Locate every Trypanosoma brucei.
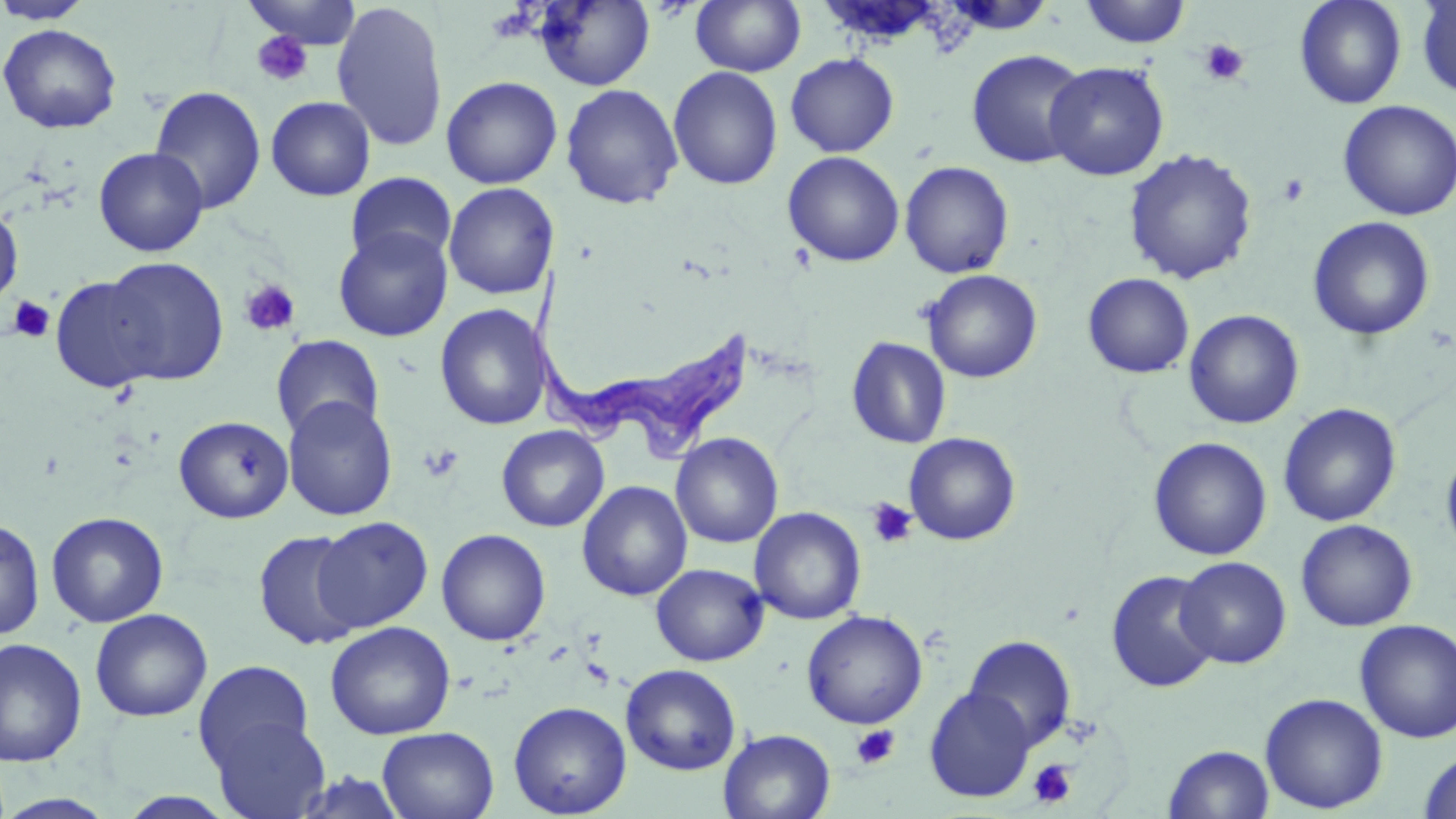

Approximate bounding boxes as (x1, y1, x2, y2) in pixels.
Trypanosoma brucei: (529, 266, 758, 463).

Uninfected red blood cell locations: (0, 0, 95, 25), (242, 0, 362, 49), (533, 0, 655, 91), (691, 0, 806, 77), (941, 0, 1055, 35), (1294, 0, 1407, 109), (1415, 0, 1456, 100), (1079, 1, 1191, 48), (332, 2, 448, 152), (0, 24, 122, 134), (966, 49, 1089, 169), (785, 53, 899, 157), (1044, 61, 1169, 181), (668, 66, 783, 190), (441, 76, 562, 189), (560, 83, 683, 210), (149, 86, 266, 215), (266, 96, 375, 201), (1338, 99, 1456, 221), (94, 147, 208, 256), (1123, 148, 1258, 285), (782, 151, 905, 267), (900, 160, 1015, 279), (345, 172, 457, 270), (443, 183, 559, 299), (0, 205, 23, 309), (1307, 216, 1435, 341), (333, 226, 453, 342), (100, 256, 229, 385), (922, 269, 1042, 383), (1082, 273, 1194, 378), (51, 276, 166, 392), (435, 303, 550, 431), (1184, 309, 1304, 429), (270, 334, 384, 439), (846, 336, 952, 449), (283, 397, 397, 521), (1278, 403, 1401, 527), (174, 415, 294, 523), (496, 425, 609, 532), (670, 432, 783, 548), (903, 432, 1020, 545), (1148, 437, 1272, 561), (1440, 448, 1456, 560), (576, 480, 692, 601), (750, 507, 866, 625), (46, 511, 169, 628), (313, 516, 433, 632), (0, 517, 45, 641), (1295, 519, 1418, 631), (252, 529, 364, 650), (436, 529, 551, 646), (1174, 556, 1291, 669), (650, 563, 768, 666), (1105, 570, 1221, 693), (89, 608, 213, 722), (801, 609, 928, 729), (1353, 618, 1456, 744), (325, 621, 456, 740), (963, 635, 1077, 750), (0, 638, 88, 767), (193, 660, 314, 774), (621, 663, 741, 775), (924, 686, 1036, 802), (1260, 692, 1388, 814), (508, 700, 632, 818), (209, 714, 331, 819), (378, 726, 499, 819), (718, 728, 836, 819), (1164, 744, 1274, 819), (1418, 750, 1456, 819), (112, 791, 243, 818), (0, 793, 118, 819). Platelet locations: (251, 30, 314, 87), (1199, 39, 1249, 85), (1278, 174, 1310, 205), (238, 279, 302, 337), (7, 295, 56, 342), (419, 444, 463, 482), (865, 497, 917, 549), (850, 724, 900, 770), (1028, 759, 1077, 808). Slide-level diagnosis: Trypanosoma brucei. Captured at 1000x magnification. May-Grünwald-Giemsa-stained preparation. Light microscopy. One field of a larger specimen. Image is 1456×819 pixels. Thin blood film.